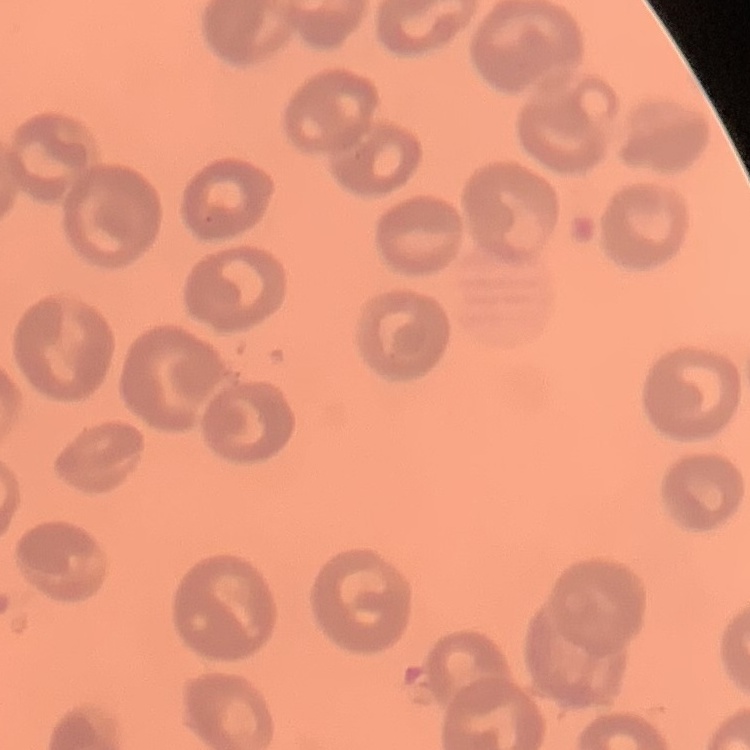
Summary:
  - Red blood cell morphology: no rouleaux formation
  - Stain: Field's or Giemsa
  - Image type: one tile cut from a larger photomicrograph
  - Preparation: thin blood smear